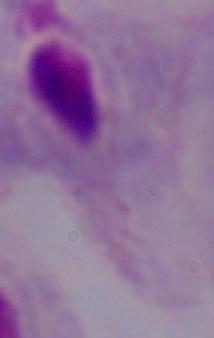
A trichomonad is shown. Captured at 1000x magnification. Micrograph.